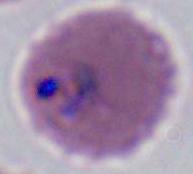
identification = Plasmodium
modality = photomicrograph
magnification = 400x or 1000x